Evaluate for malaria.
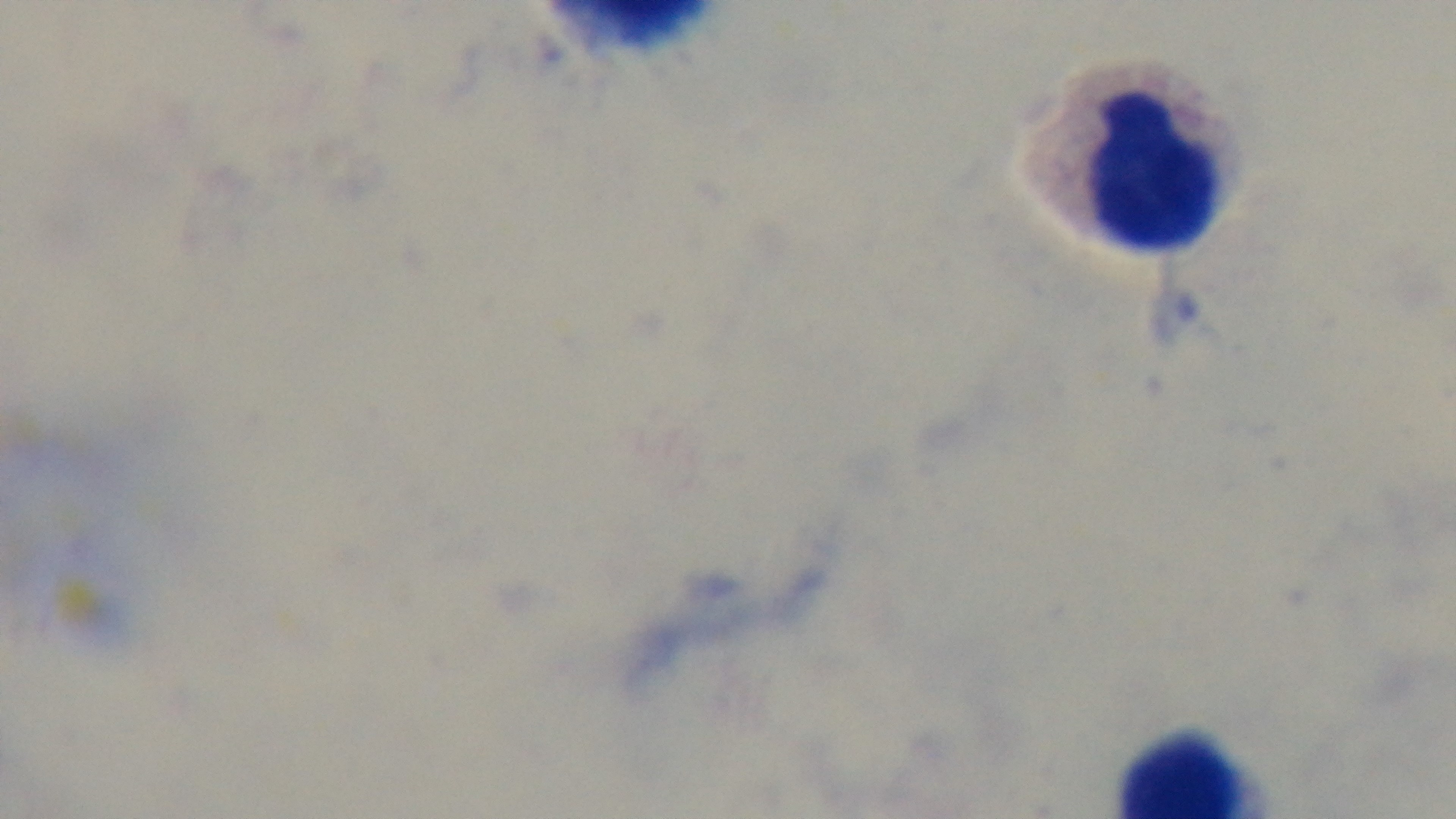
Negative.

Summary:
  - Field of view: single
  - Objective: 100x oil immersion
  - Capture: mounted 4K digital camera
  - Stain: Giemsa
  - Preparation: thick smear
  - Modality: light microscopy